Assess this cell for malaria.
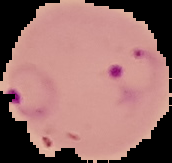

It is parasitized.

image type = segmented cell region on a black background
preparation = thin blood film
image size = 172×163 pixels